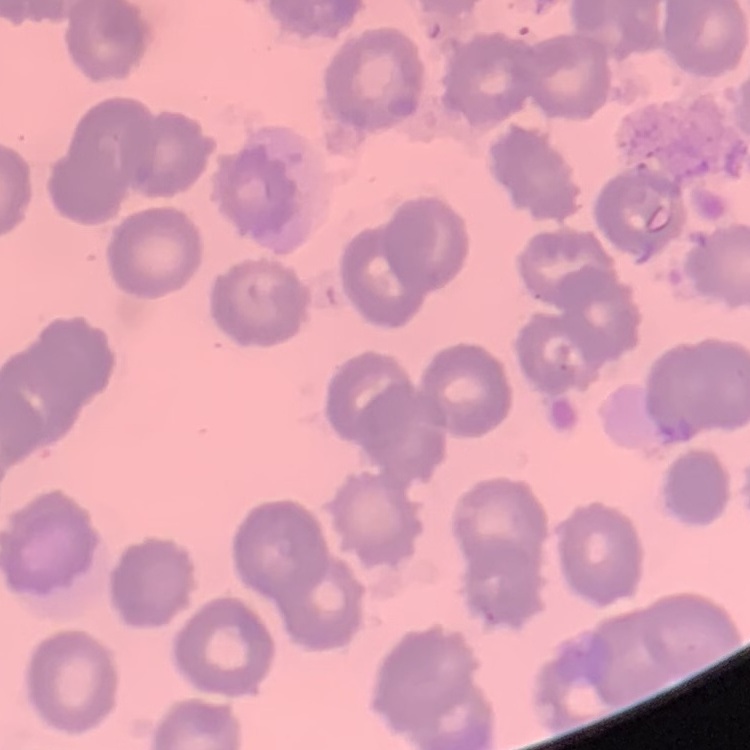 The red blood cells exhibit no rouleaux formation. Field's or Giemsa stain. One tile cut from a larger photomicrograph. Thin peripheral smear.